Identify the blood parasite species.
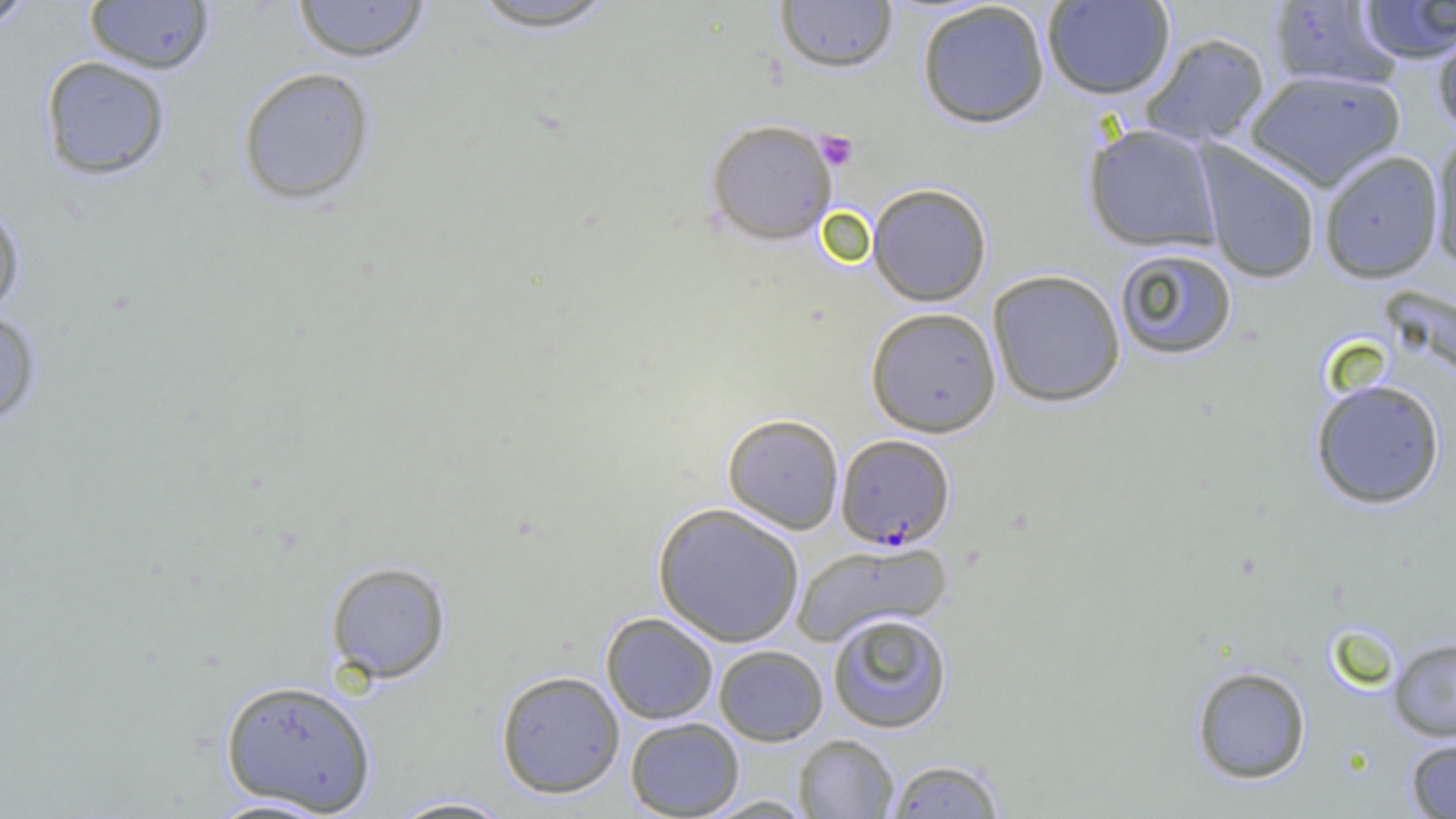

Plasmodium falciparum.

Approximate bounding boxes as (x1, y1, x2, y2) in pixels. Platelet locations: (815, 131, 859, 171). Plasmodium falciparum-infected red blood cell locations: (836, 434, 955, 549). Uninfected red blood cell locations: (0, 0, 38, 33), (292, 0, 431, 63), (774, 0, 899, 74), (84, 1, 215, 75), (462, 1, 622, 33), (916, 1, 1050, 129), (1042, 1, 1175, 99), (1267, 1, 1403, 91), (1355, 1, 1456, 64), (1431, 18, 1456, 136), (1140, 32, 1271, 147), (39, 55, 171, 181), (236, 66, 377, 206), (1245, 69, 1405, 191), (705, 118, 838, 245), (1083, 124, 1222, 252), (1429, 128, 1456, 269), (1195, 143, 1321, 285), (1319, 150, 1444, 283), (868, 183, 992, 306), (0, 199, 25, 319), (1113, 247, 1237, 360), (987, 269, 1126, 407), (865, 306, 1002, 437), (0, 307, 43, 430), (1310, 378, 1446, 510), (722, 413, 844, 534), (653, 502, 805, 647), (790, 540, 952, 646), (325, 560, 452, 684), (600, 612, 719, 724), (827, 612, 953, 733), (1388, 637, 1456, 741), (713, 644, 828, 746), (1191, 665, 1312, 784), (495, 670, 626, 799), (219, 678, 377, 815), (625, 717, 745, 818), (793, 734, 899, 818), (1405, 736, 1456, 818), (887, 759, 1005, 818), (385, 795, 517, 818), (699, 795, 816, 818), (201, 796, 342, 818). Image is 1456×819 pixels. Captured at 1000x magnification. Thin blood smear. One field of a larger specimen. Light microscopy.